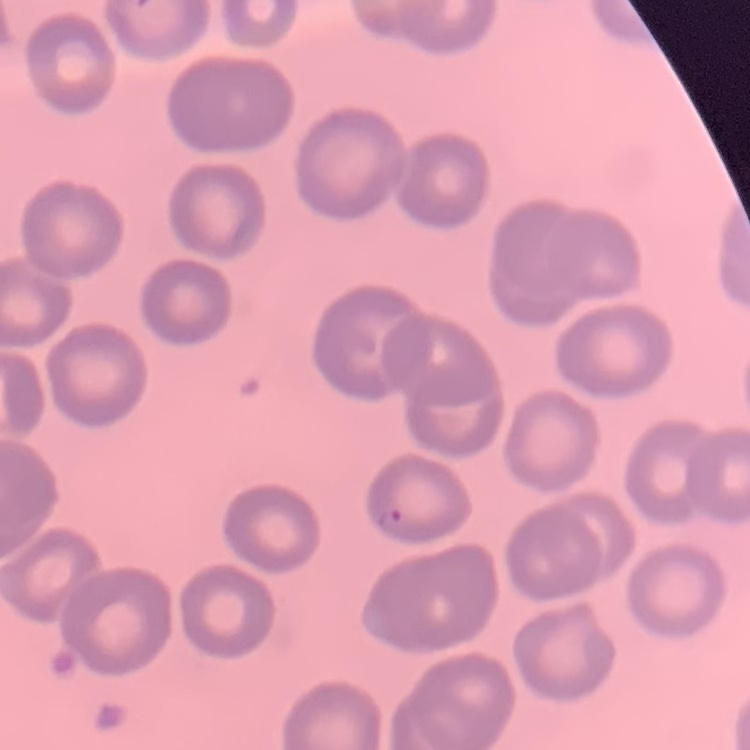
The red blood cells exhibit no rouleaux formation. Stained with either Field's or Giemsa. Square crop of a larger photomicrograph. Thin blood smear.